Locate every Plasmodium parasite.
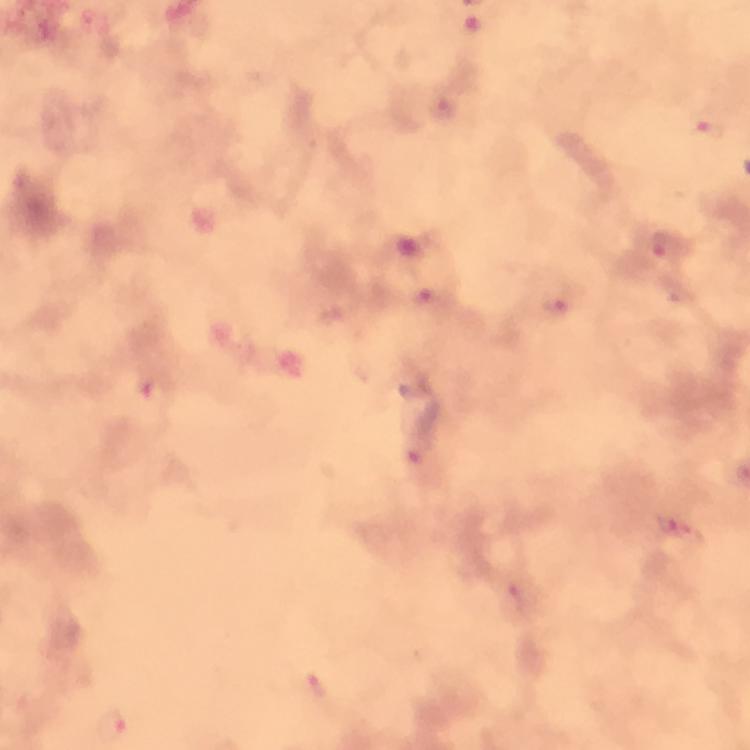
Approximate object centers, in pixels from the top-left corner.
Plasmodium parasites: (x=446, y=108), (x=706, y=126), (x=663, y=246), (x=556, y=307), (x=160, y=393), (x=417, y=454), (x=679, y=530), (x=316, y=685), (x=111, y=723).

A crop from one field of view. Image is 750×750 pixels. Giemsa stain. At 100x magnification. From a malaria diagnostic workup. Thick blood film. Photographed with a smartphone mounted on the microscope. Immersion oil applied.